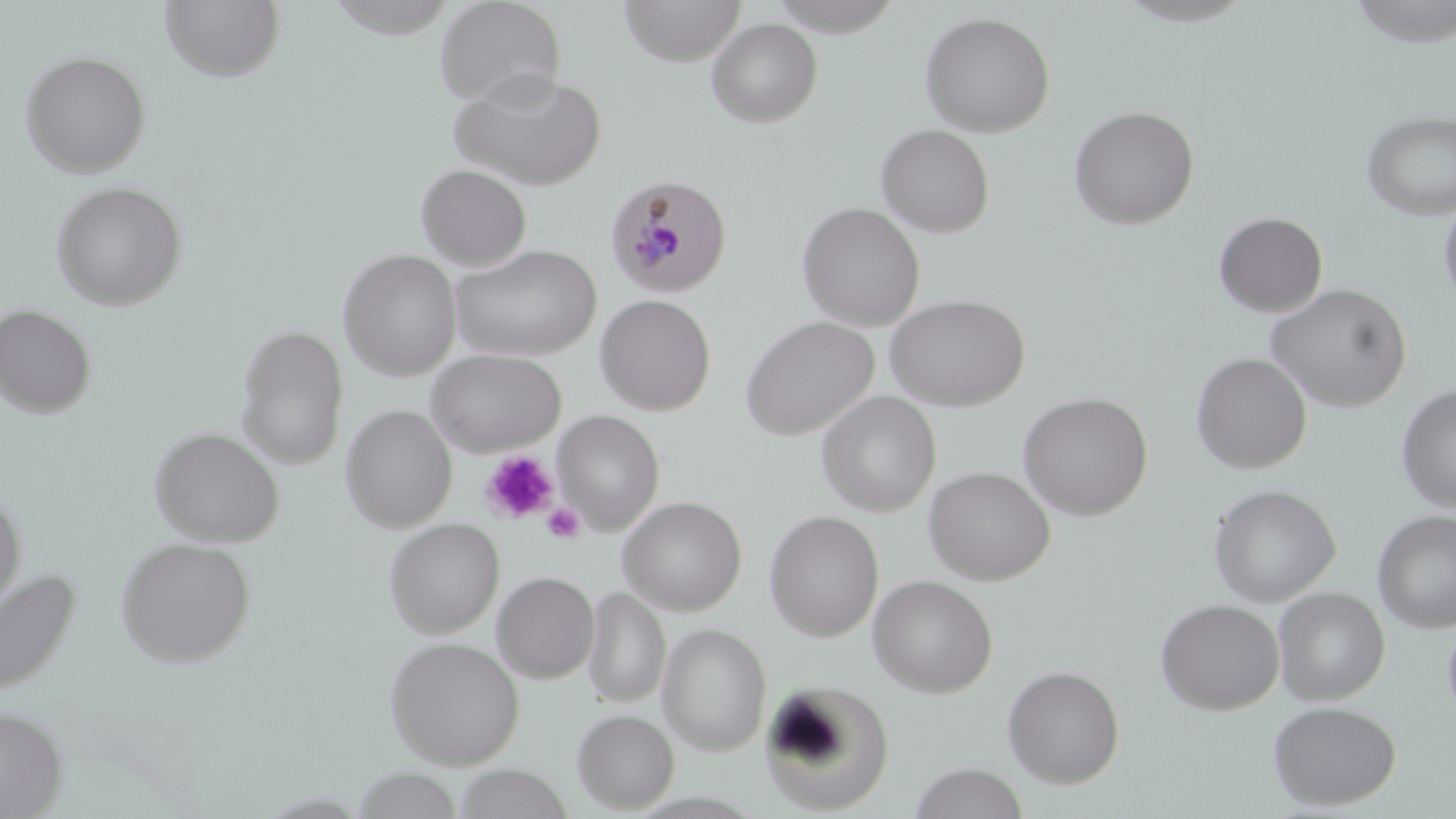

slide_level_diagnosis: Plasmodium malariae
uninfected_red_blood_cell_locations: 'approximate bounding boxes as (x1, y1, x2, y2) in pixels: (159, 0, 286, 83), (434, 0, 567, 109), (619, 0, 746, 65), (765, 0, 904, 36), (1114, 0, 1259, 27), (324, 1, 461, 40), (919, 11, 1056, 137), (706, 18, 823, 128), (20, 50, 151, 177), (449, 69, 607, 191), (1068, 105, 1200, 230), (1361, 109, 1456, 221), (875, 124, 995, 238), (416, 164, 532, 270), (51, 180, 187, 310), (1439, 196, 1456, 310), (797, 202, 925, 331), (1213, 211, 1328, 317), (448, 244, 602, 362), (339, 249, 462, 379), (1266, 283, 1412, 413), (595, 294, 716, 415), (885, 294, 1031, 410), (0, 303, 97, 419), (739, 316, 879, 440), (235, 323, 349, 469), (425, 348, 567, 455), (1192, 352, 1312, 473), (1397, 384, 1456, 513), (1018, 391, 1154, 520), (817, 392, 941, 517), (341, 405, 456, 532), (554, 411, 664, 534), (149, 426, 284, 546), (924, 466, 1055, 585), (1208, 483, 1341, 605), (0, 486, 27, 615), (618, 496, 747, 616), (1373, 509, 1456, 633), (764, 510, 884, 641), (384, 518, 504, 637), (116, 536, 256, 667), (0, 565, 82, 699), (492, 571, 599, 682), (867, 575, 998, 698), (583, 586, 670, 708), (1273, 587, 1390, 705), (1155, 598, 1284, 715), (1442, 617, 1456, 725), (658, 622, 771, 755), (385, 636, 525, 768), (1003, 664, 1125, 788), (760, 680, 893, 814), (1268, 700, 1402, 810), (0, 706, 67, 818), (572, 708, 678, 813), (909, 762, 1029, 819), (450, 765, 576, 819), (351, 767, 466, 819)'
platelet_locations: 'approximate bounding boxes as (x1, y1, x2, y2) in pixels: (480, 450, 559, 525), (542, 502, 585, 544)'
modality: optical microscopy
magnification: 1000x
stain: May-Grünwald-Giemsa
preparation: thin blood smear
image_size: 1456×819 pixels
field_of_view: one of a larger specimen
plasmodium_malariae_infected_red_blood_cell_locations: 'approximate bounding boxes as (x1, y1, x2, y2) in pixels: (604, 173, 734, 299)'